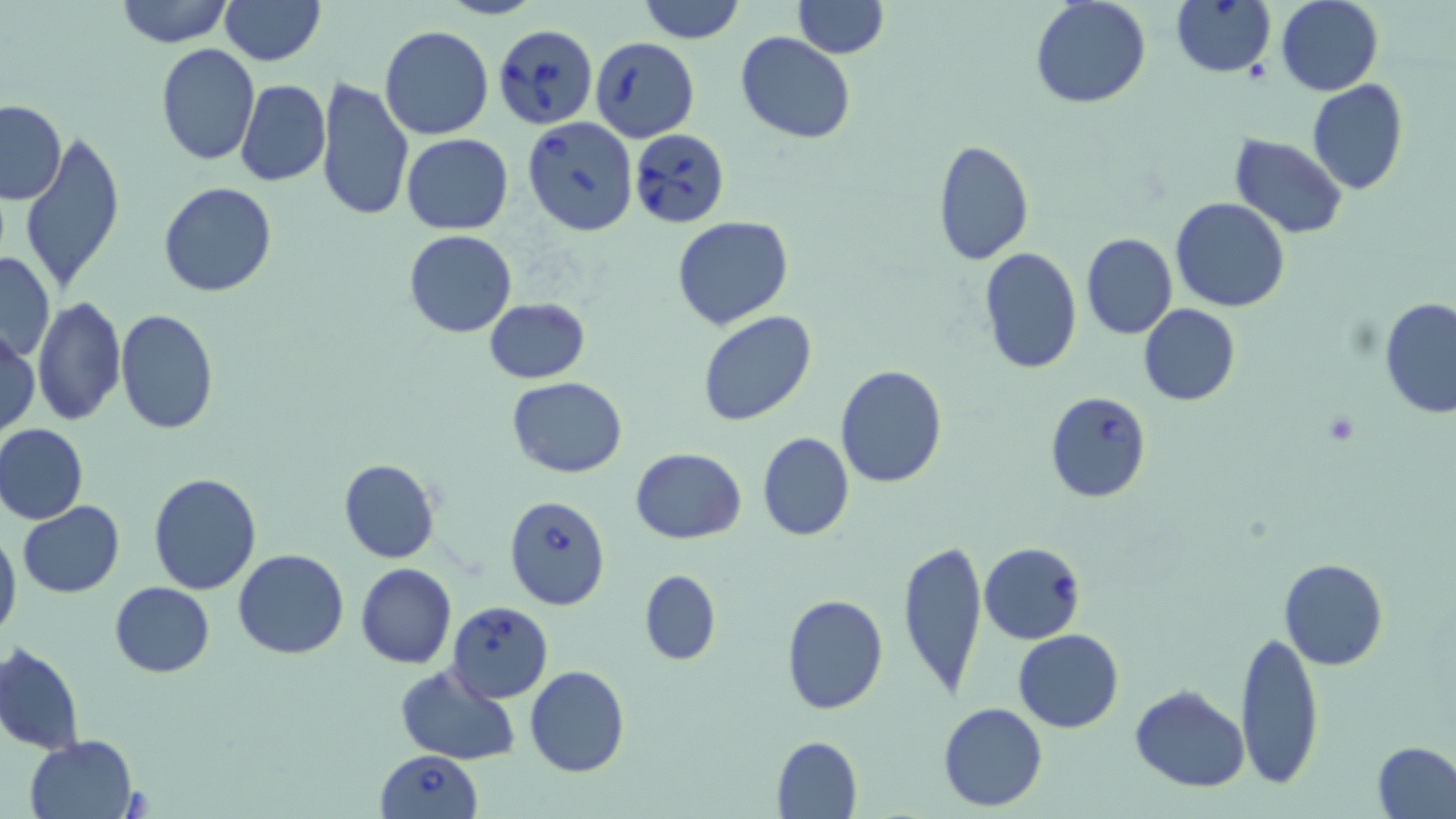
{
  "slide_level_diagnosis": "Babesia divergens",
  "uninfected_red_blood_cell_locations": "approximate bounding boxes as [x1, y1, x2, y2] in pixels: [113, 0, 234, 48], [220, 0, 324, 65], [638, 0, 745, 44], [792, 0, 887, 57], [1030, 0, 1151, 109], [1276, 1, 1383, 95], [379, 26, 495, 139], [736, 33, 855, 143], [154, 45, 260, 166], [315, 77, 414, 222], [235, 80, 330, 187], [1306, 80, 1407, 196], [0, 100, 67, 205], [17, 129, 127, 295], [401, 133, 513, 234], [1229, 134, 1347, 238], [930, 139, 1035, 265], [158, 182, 277, 297], [1171, 196, 1290, 313], [672, 216, 794, 332], [404, 230, 516, 339], [1080, 233, 1178, 339], [978, 247, 1081, 373], [0, 253, 54, 363], [32, 295, 125, 428], [1379, 298, 1456, 418], [482, 299, 590, 383], [1138, 303, 1240, 406], [115, 310, 219, 433], [698, 311, 816, 427], [1, 328, 40, 439], [834, 364, 948, 489], [507, 377, 627, 478], [1, 424, 87, 524], [757, 432, 853, 542], [630, 449, 747, 543], [337, 459, 441, 563], [148, 471, 261, 595], [18, 502, 124, 598], [0, 528, 22, 644], [897, 538, 988, 700], [232, 549, 348, 659], [1278, 557, 1388, 670], [355, 564, 456, 668], [639, 570, 721, 664], [110, 581, 215, 677], [780, 593, 888, 715], [1236, 628, 1324, 790], [1014, 630, 1124, 732], [1, 642, 85, 754], [395, 663, 520, 764], [525, 666, 630, 778], [1129, 684, 1250, 793], [938, 702, 1048, 811], [23, 735, 141, 819], [771, 735, 862, 817], [1374, 741, 1456, 817]",
  "babesia_divergens_infected_red_blood_cell_locations": "approximate bounding boxes as [x1, y1, x2, y2] in pixels: [1171, 0, 1276, 77], [492, 23, 600, 130], [590, 35, 700, 143], [522, 117, 638, 237], [630, 128, 728, 226], [1045, 391, 1152, 503], [504, 495, 610, 611], [979, 542, 1086, 644], [445, 602, 554, 703], [375, 750, 483, 819]",
  "preparation": "thin blood film",
  "magnification": "1000x",
  "image_size": "1456×819 pixels",
  "modality": "optical microscopy",
  "field_of_view": "single",
  "stain": "May-Grünwald-Giemsa"
}